Describe the morphology of the erythrocytes.
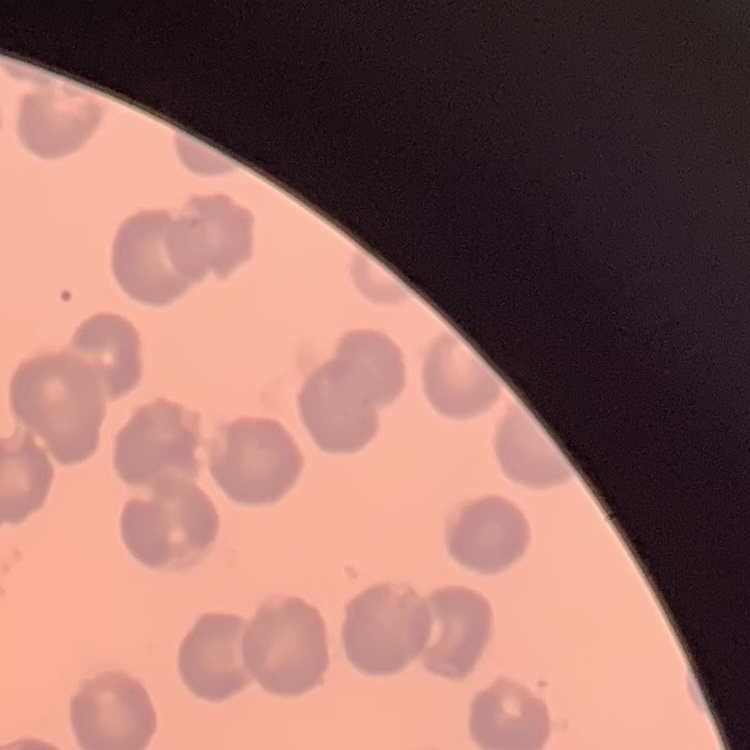
No rouleaux formation.

Stained with either Field's or Giemsa. Square crop of a larger photomicrograph. Thin blood film.